Identify the preparation type.
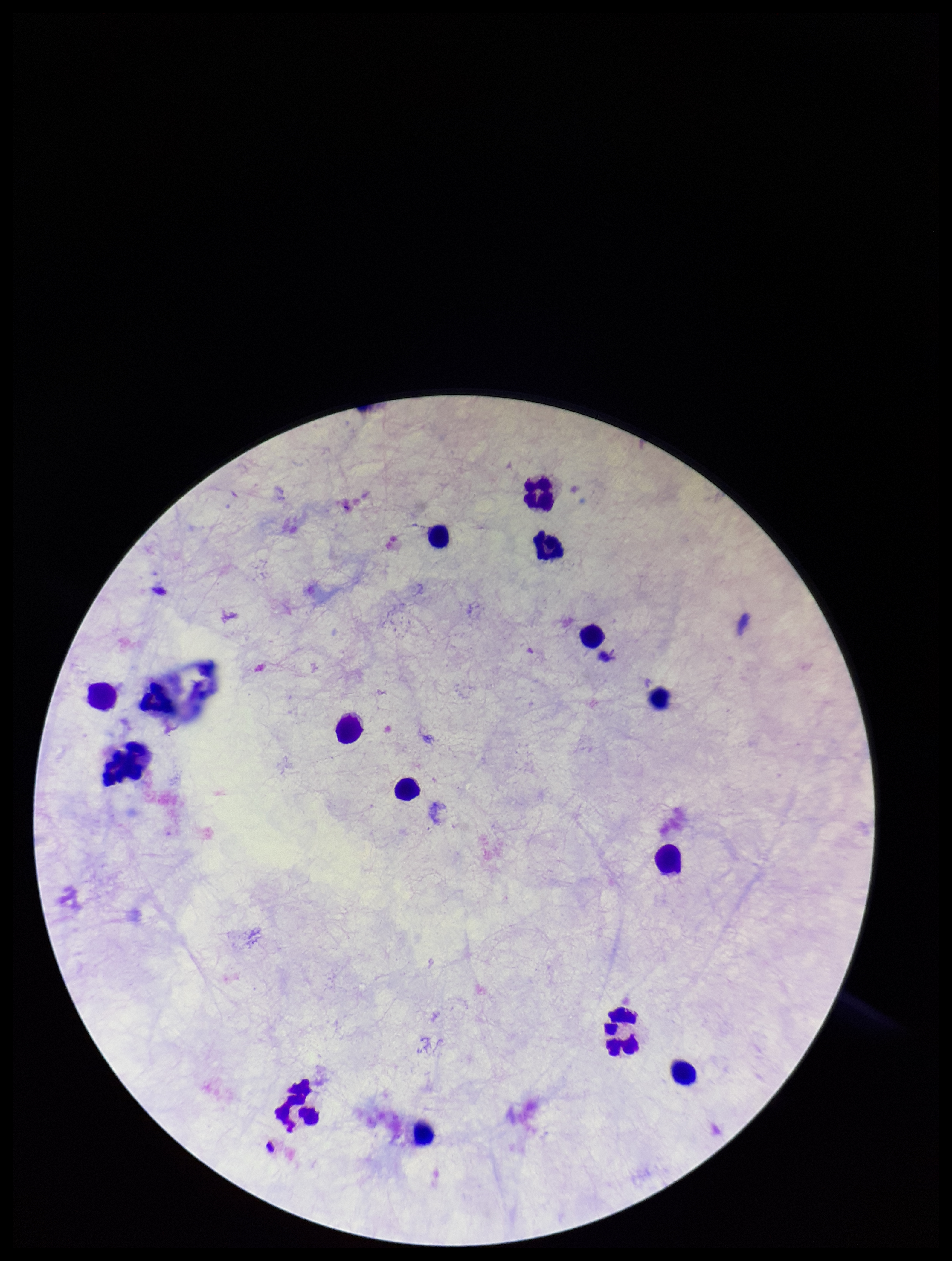

Thick.

Plasmodium parasites: none identified. Leukocyte count: 14. Giemsa stain. Patient malaria status: negative. Single field of view. Photographed through the microscope eyepiece with a smartphone camera. Image is 952×1261 pixels. Parasite count: 0.